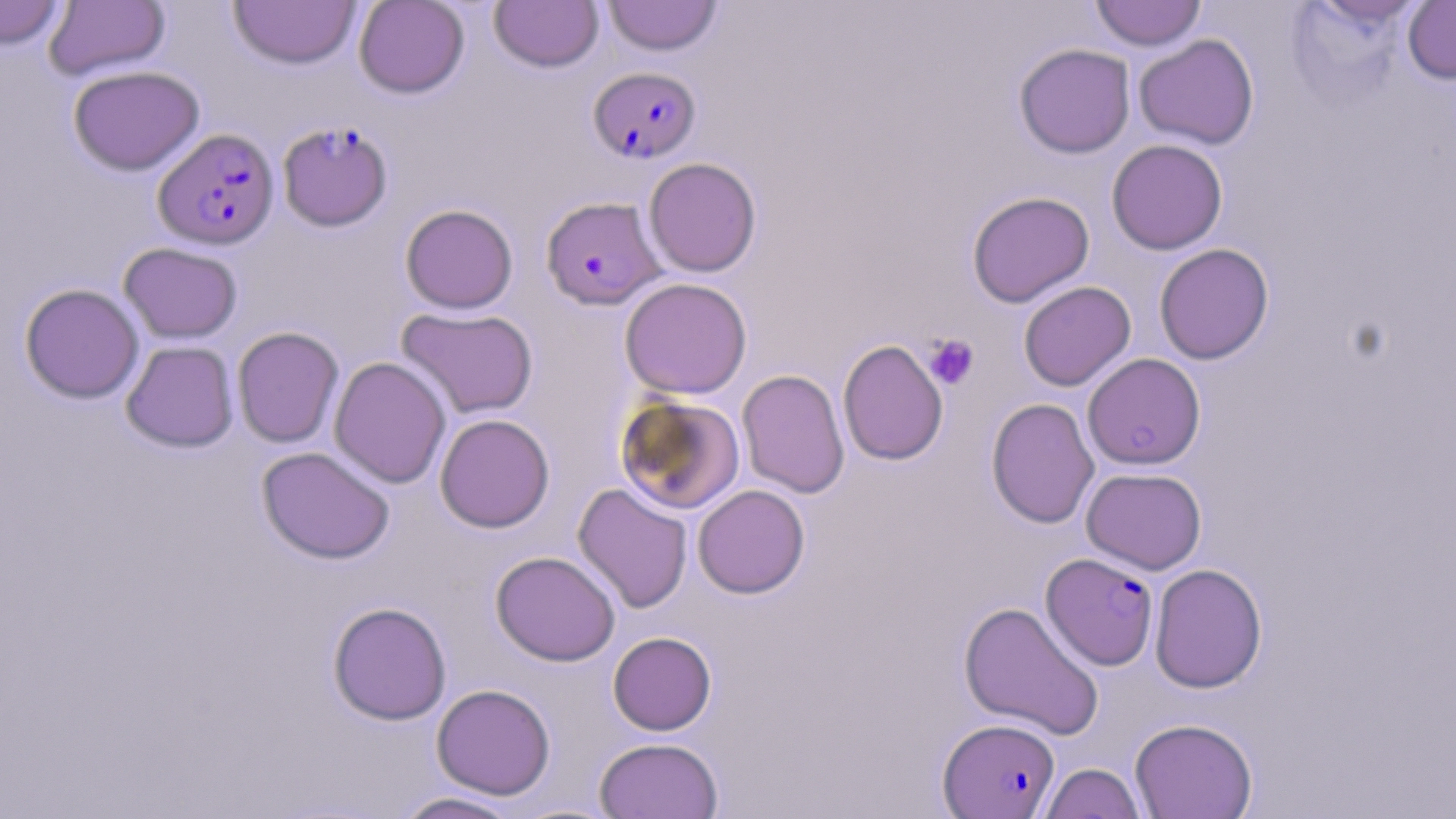
slide-level diagnosis = Plasmodium falciparum
uninfected red blood cell locations = approximate bounding boxes as named x1/y1/x2/y2 corners in pixels: (x1=0, y1=0, x2=67, y2=49), (x1=353, y1=0, x2=470, y2=98), (x1=490, y1=0, x2=604, y2=72), (x1=603, y1=0, x2=722, y2=56), (x1=1090, y1=0, x2=1206, y2=51), (x1=1403, y1=0, x2=1456, y2=85), (x1=43, y1=1, x2=171, y2=81), (x1=228, y1=1, x2=360, y2=70), (x1=1134, y1=34, x2=1260, y2=150), (x1=1013, y1=43, x2=1136, y2=159), (x1=68, y1=65, x2=205, y2=176), (x1=1106, y1=139, x2=1228, y2=255), (x1=643, y1=157, x2=762, y2=277), (x1=966, y1=190, x2=1095, y2=307), (x1=400, y1=203, x2=518, y2=314), (x1=119, y1=242, x2=242, y2=343), (x1=1154, y1=243, x2=1274, y2=365), (x1=619, y1=277, x2=752, y2=399), (x1=1018, y1=281, x2=1136, y2=391), (x1=19, y1=283, x2=144, y2=404), (x1=396, y1=307, x2=538, y2=419), (x1=232, y1=326, x2=344, y2=448), (x1=837, y1=339, x2=948, y2=466), (x1=121, y1=340, x2=239, y2=453), (x1=1082, y1=353, x2=1206, y2=470), (x1=329, y1=357, x2=451, y2=488), (x1=736, y1=369, x2=850, y2=499), (x1=615, y1=394, x2=745, y2=514), (x1=986, y1=398, x2=1100, y2=529), (x1=434, y1=413, x2=555, y2=533), (x1=256, y1=446, x2=395, y2=564), (x1=1081, y1=467, x2=1207, y2=575), (x1=573, y1=483, x2=693, y2=613), (x1=692, y1=484, x2=810, y2=598), (x1=490, y1=551, x2=620, y2=666), (x1=1149, y1=563, x2=1268, y2=693), (x1=958, y1=600, x2=1104, y2=740), (x1=327, y1=601, x2=452, y2=725), (x1=608, y1=631, x2=716, y2=735), (x1=431, y1=683, x2=556, y2=800), (x1=1130, y1=717, x2=1258, y2=818), (x1=594, y1=737, x2=723, y2=819), (x1=1039, y1=762, x2=1146, y2=819), (x1=391, y1=791, x2=527, y2=818)
field of view = one of a larger specimen
image size = 1456×819 pixels
Plasmodium falciparum-infected red blood cell locations = approximate bounding boxes as named x1/y1/x2/y2 corners in pixels: (x1=588, y1=66, x2=701, y2=164), (x1=277, y1=120, x2=393, y2=232), (x1=153, y1=127, x2=280, y2=250), (x1=541, y1=195, x2=665, y2=311), (x1=1040, y1=552, x2=1159, y2=670), (x1=938, y1=717, x2=1060, y2=818)
stain = May-Grünwald-Giemsa
magnification = 1000x
platelet locations = approximate bounding boxes as named x1/y1/x2/y2 corners in pixels: (x1=924, y1=335, x2=978, y2=389)
preparation = thin blood film
modality = optical microscopy